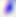
modality = micrograph
magnification = 400x
identification = Toxoplasma gondii